Classify this cell by malaria status.
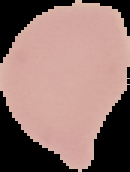
It is uninfected.

preparation = thin blood film
image type = segmented cell region on a black background
image size = 130×172 pixels